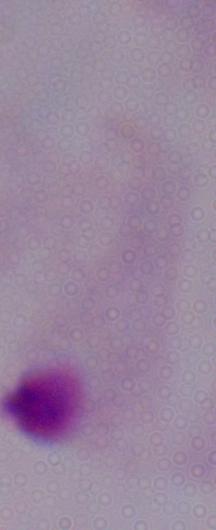 A trichomonad is shown. Captured at 1000x magnification. Photomicrograph.